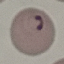

result = malaria parasites detected
stain = Giemsa
preparation = thin smear
image type = cell patch, automatically extracted from a larger field of view and resized to 64 × 64 pixels
capture = smartphone camera at the microscope eyepiece